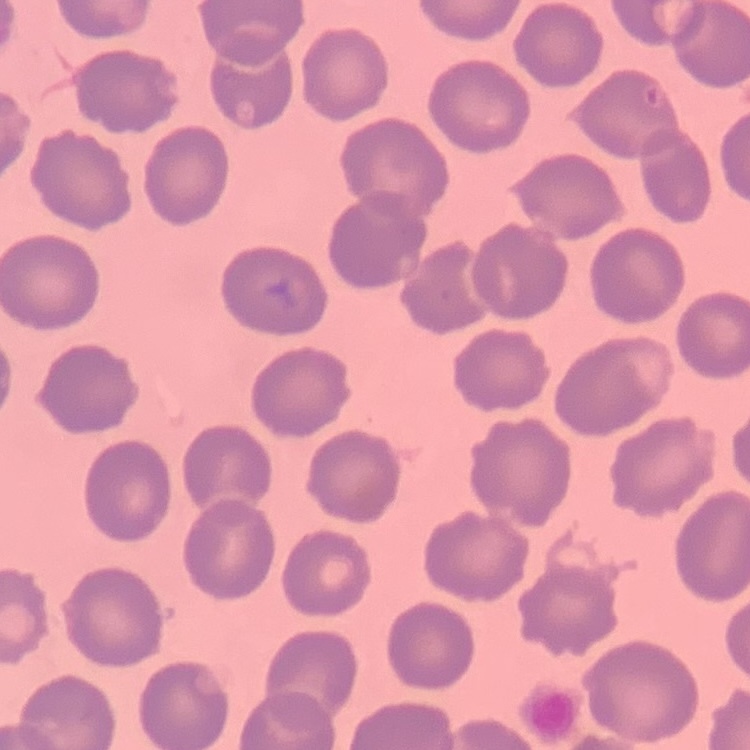
Summary:
  - Erythrocyte morphology: no rouleaux formation
  - Stain: Field's or Giemsa
  - Image type: one tile cut from a larger photomicrograph
  - Preparation: thin blood smear